Outline each uninfected red blood cell.
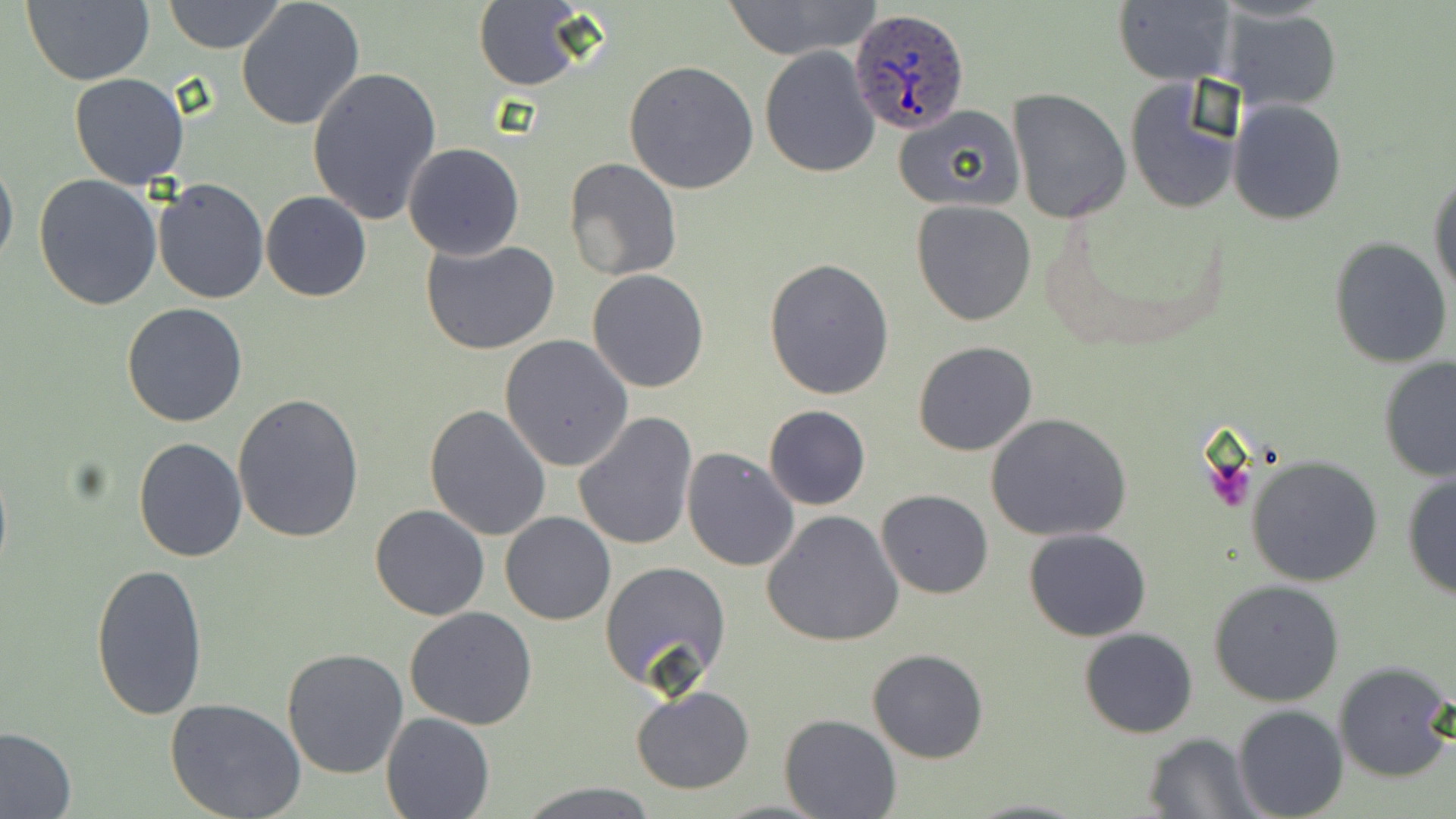
Approximate bounding boxes as named x1/y1/x2/y2 corners in pixels.
Uninfected red blood cells: (x1=21, y1=0, x2=155, y2=86), (x1=163, y1=0, x2=287, y2=54), (x1=718, y1=0, x2=883, y2=60), (x1=236, y1=1, x2=366, y2=134), (x1=473, y1=1, x2=589, y2=89), (x1=1114, y1=2, x2=1237, y2=85), (x1=1227, y1=10, x2=1339, y2=109), (x1=759, y1=46, x2=881, y2=179), (x1=624, y1=60, x2=759, y2=194), (x1=306, y1=64, x2=443, y2=226), (x1=68, y1=73, x2=191, y2=190), (x1=1124, y1=78, x2=1244, y2=216), (x1=1006, y1=89, x2=1132, y2=225), (x1=1229, y1=99, x2=1347, y2=224), (x1=892, y1=104, x2=1025, y2=214), (x1=403, y1=142, x2=524, y2=258), (x1=0, y1=153, x2=18, y2=272), (x1=564, y1=156, x2=682, y2=280), (x1=1428, y1=168, x2=1455, y2=300), (x1=33, y1=174, x2=163, y2=310), (x1=152, y1=178, x2=270, y2=303), (x1=143, y1=181, x2=260, y2=426), (x1=261, y1=191, x2=371, y2=302), (x1=912, y1=199, x2=1038, y2=326), (x1=1329, y1=236, x2=1453, y2=370), (x1=420, y1=237, x2=561, y2=355), (x1=763, y1=258, x2=896, y2=400), (x1=587, y1=269, x2=710, y2=393), (x1=121, y1=302, x2=249, y2=428), (x1=500, y1=334, x2=634, y2=470), (x1=913, y1=341, x2=1038, y2=457), (x1=1378, y1=356, x2=1456, y2=484), (x1=231, y1=394, x2=366, y2=545), (x1=424, y1=404, x2=551, y2=542), (x1=764, y1=406, x2=870, y2=510), (x1=574, y1=412, x2=698, y2=551), (x1=986, y1=412, x2=1133, y2=541), (x1=134, y1=436, x2=247, y2=561), (x1=681, y1=448, x2=799, y2=572), (x1=1244, y1=455, x2=1385, y2=588), (x1=1401, y1=472, x2=1456, y2=600), (x1=876, y1=488, x2=993, y2=599), (x1=370, y1=504, x2=490, y2=621), (x1=762, y1=510, x2=904, y2=647), (x1=500, y1=511, x2=616, y2=625), (x1=1023, y1=529, x2=1151, y2=643), (x1=91, y1=556, x2=209, y2=722), (x1=598, y1=561, x2=732, y2=693), (x1=1208, y1=579, x2=1346, y2=706), (x1=404, y1=606, x2=538, y2=731), (x1=1079, y1=627, x2=1198, y2=738), (x1=282, y1=646, x2=409, y2=778), (x1=867, y1=648, x2=988, y2=764), (x1=1333, y1=661, x2=1455, y2=783), (x1=632, y1=684, x2=755, y2=795), (x1=165, y1=697, x2=307, y2=819), (x1=1232, y1=706, x2=1348, y2=819), (x1=382, y1=712, x2=494, y2=818), (x1=778, y1=714, x2=902, y2=819), (x1=0, y1=726, x2=77, y2=819), (x1=1139, y1=732, x2=1260, y2=816), (x1=520, y1=782, x2=658, y2=818), (x1=965, y1=798, x2=1093, y2=818), (x1=715, y1=799, x2=832, y2=817).

Summary:
  - Plasmodium ovale-infected red blood cell locations: (x1=850, y1=7, x2=972, y2=137)
  - Slide-level diagnosis: Plasmodium ovale
  - Image size: 1456×819 pixels
  - Modality: light microscopy
  - Stain: May-Grünwald-Giemsa
  - Magnification: 1000x
  - Preparation: thin blood smear
  - Field of view: one of a larger specimen